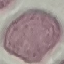
Summary:
  - Malaria status: uninfected
  - Image type: cell patch, automatically extracted from a larger field of view and resized to 64 × 64 pixels
  - Preparation: thin blood film
  - Capture: smartphone through the microscope eyepiece
  - Stain: Giemsa